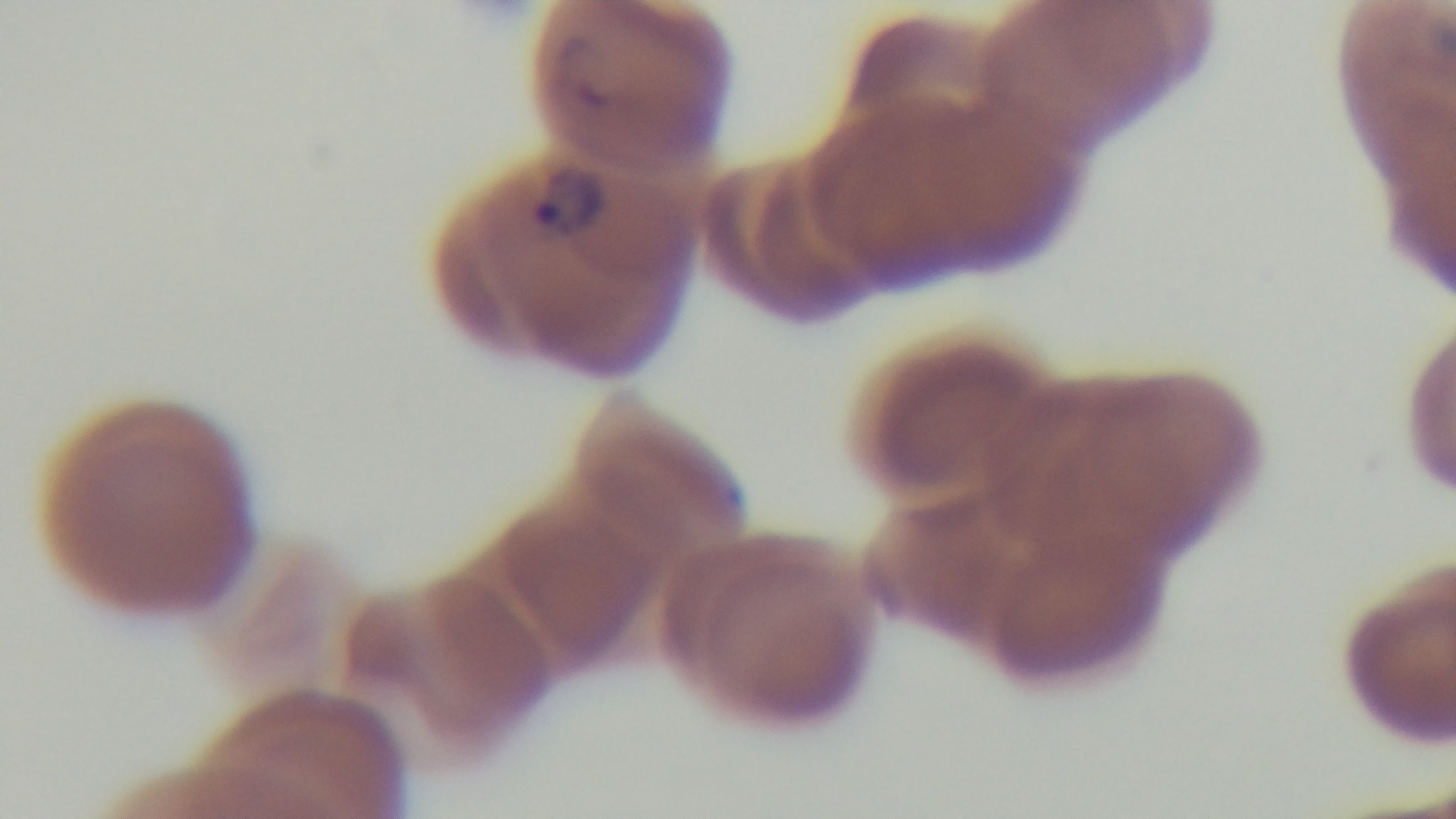
Summary:
  - Malaria status: positive
  - Capture: mounted 4K digital camera
  - Field of view: single
  - Stain: Giemsa
  - Objective: 100x oil immersion
  - Modality: light microscopy
  - Preparation: thin smear